Give the preparation type.
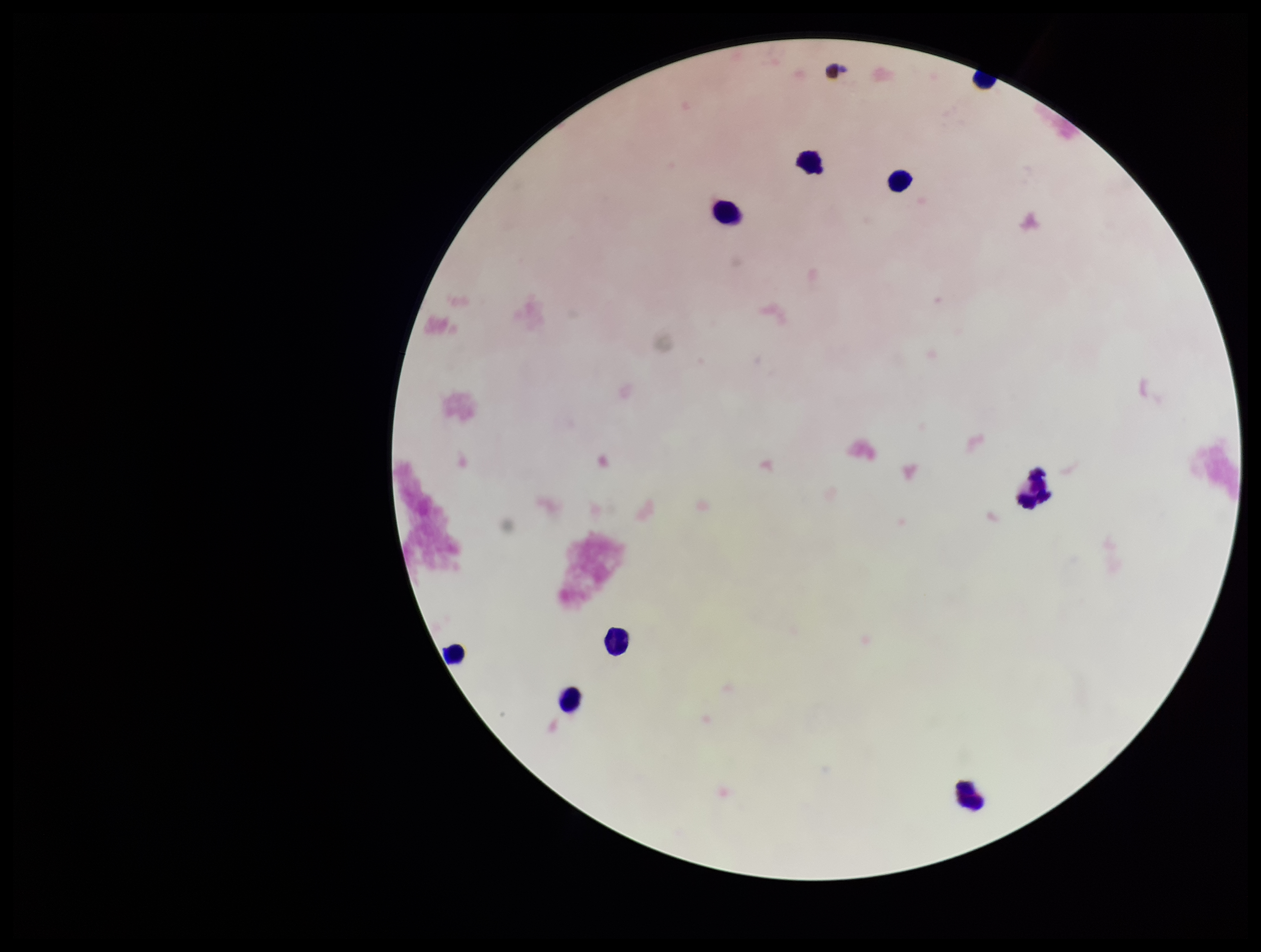
A thick smear.

Smartphone photograph taken through the eyepiece of a microscope. Parasite count: 0. Stained with Giemsa. Leukocyte count: 9. Plasmodium parasites: none detected. Single field of view. Patient malaria status: negative. Image is 1261×952 pixels.